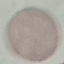 Result: no malaria parasites seen. Photographed with a smartphone camera at the microscope eyepiece. Cell patch, automatically extracted from a larger field of view and resized to 64 × 64 pixels. Giemsa-stained preparation. Thin blood film.